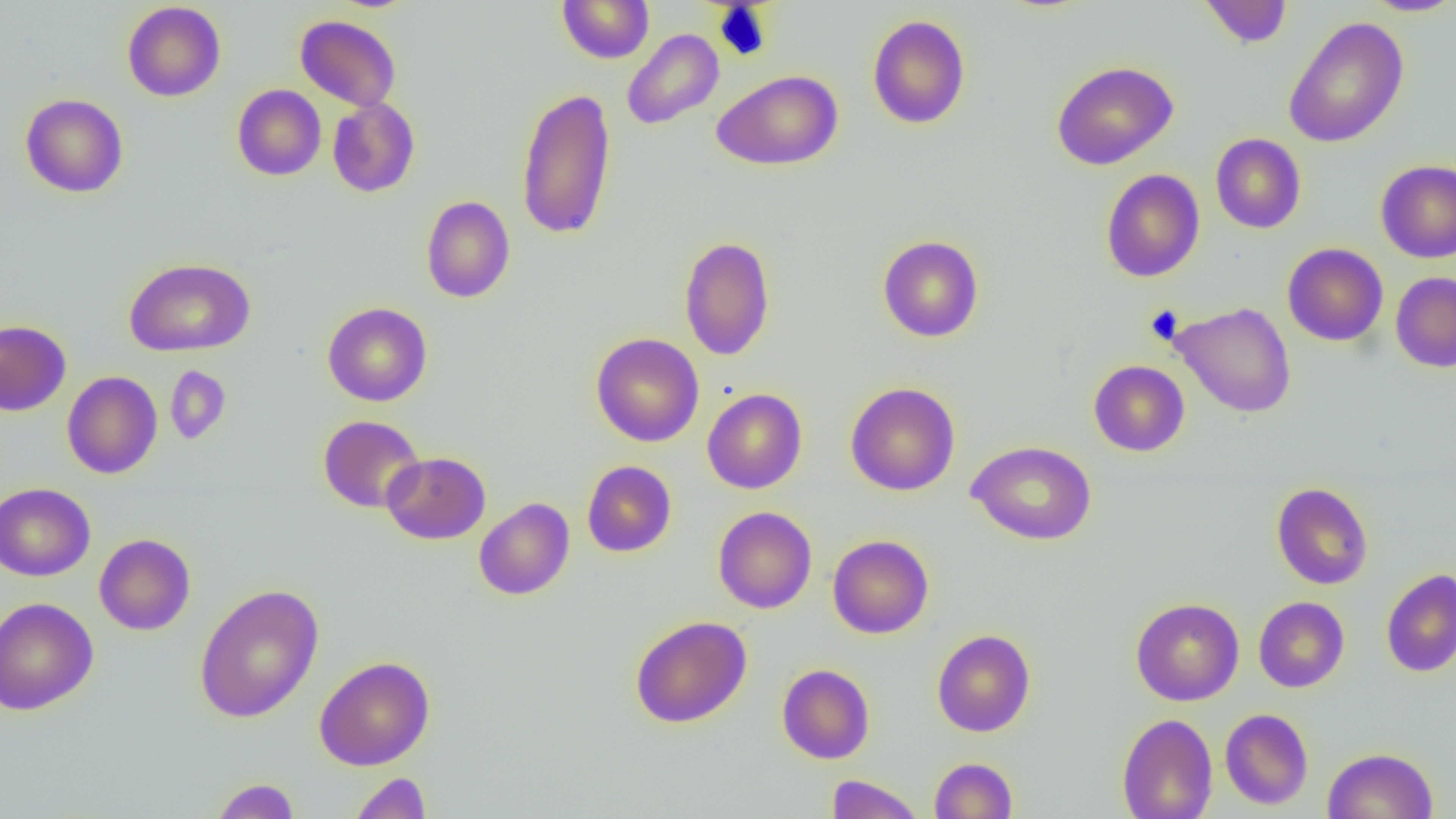
Summary:
  - Coordinate format: approximate bounding boxes as (x1, y1, x2, y2) in pixels
  - Uninfected red blood cell locations: (1199, 0, 1293, 48), (1361, 0, 1456, 17), (122, 1, 226, 102), (557, 1, 654, 63), (867, 14, 971, 130), (295, 15, 401, 111), (1282, 15, 1410, 149), (622, 29, 724, 130), (1051, 60, 1178, 170), (712, 70, 844, 171), (232, 84, 326, 181), (515, 86, 618, 240), (20, 93, 129, 198), (327, 98, 420, 198), (1210, 133, 1306, 234), (1375, 160, 1456, 262), (1101, 169, 1204, 283), (421, 196, 515, 303), (877, 235, 984, 342), (679, 236, 776, 361), (1282, 243, 1388, 345), (124, 257, 256, 357), (1390, 272, 1456, 372), (1171, 301, 1297, 418), (322, 302, 432, 406), (0, 319, 71, 416), (591, 333, 704, 447), (1088, 360, 1190, 456), (165, 365, 231, 445), (62, 371, 162, 479), (845, 381, 960, 496), (702, 388, 807, 493), (318, 415, 426, 513), (967, 440, 1097, 545), (381, 451, 491, 544), (582, 460, 677, 557), (0, 482, 95, 581), (1271, 482, 1374, 590), (474, 497, 574, 600), (713, 506, 817, 613), (94, 533, 196, 635), (827, 535, 933, 638), (1381, 568, 1456, 677), (194, 584, 324, 722), (1253, 596, 1349, 692), (0, 597, 99, 715), (1130, 597, 1244, 705), (630, 615, 752, 728), (931, 628, 1035, 737), (314, 655, 435, 771), (776, 663, 875, 764), (1219, 708, 1313, 810), (1117, 713, 1217, 819), (1323, 747, 1438, 819), (929, 757, 1018, 818), (348, 772, 432, 819), (826, 774, 924, 818), (210, 778, 301, 819)
  - Slide-level diagnosis: negative for blood parasites
  - Image size: 1456×819 pixels
  - Modality: light microscopy
  - Magnification: 1000x
  - Field of view: one of a larger specimen
  - Preparation: thin blood film